Point out each malaria parasite.
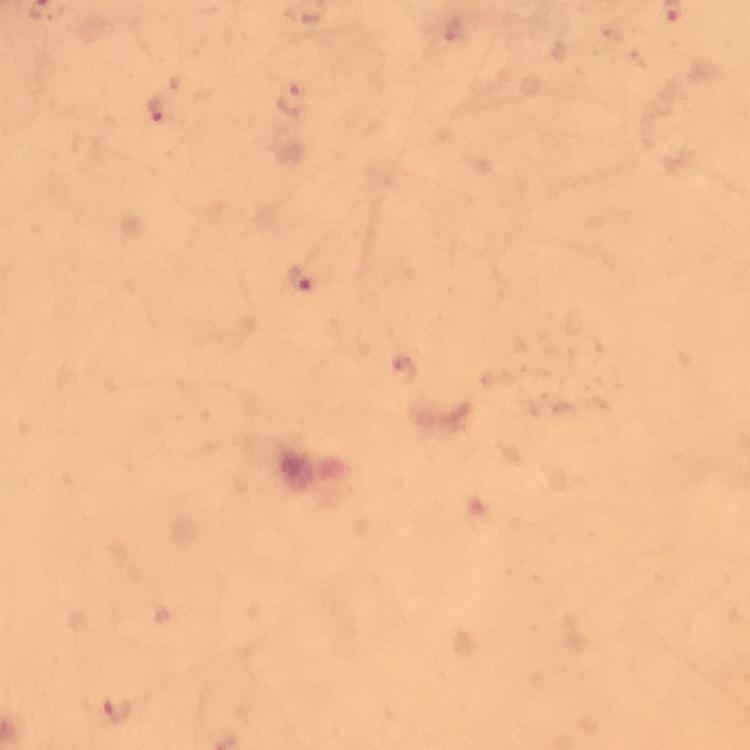
Approximate object centers, in pixels from the top-left corner.
Malaria parasites: (x=292, y=101), (x=160, y=111), (x=300, y=278), (x=117, y=713).

Summary:
  - Preparation: thick blood film
  - Context: from a malaria diagnostic workup
  - Magnification: 100x
  - Immersion oil: applied
  - Capture: smartphone camera through the microscope
  - Stain: Giemsa
  - Image size: 750×750 pixels
  - Cropped from: a single field of view